Classify this cell by malaria status.
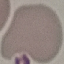
It is uninfected.

image type = cell patch, automatically extracted from a larger field of view and resized to 64 × 64 pixels
preparation = thin smear
capture = smartphone camera at the microscope eyepiece
stain = Giemsa